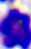
Summary:
  - Identification: white blood cell
  - Modality: photomicrograph
  - Magnification: 400x